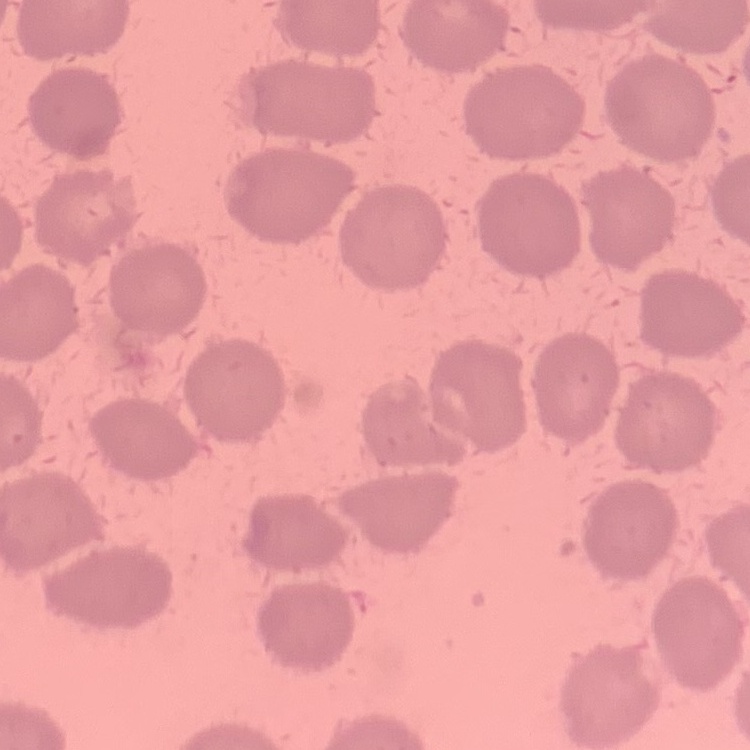 The red blood cells exhibit no rouleaux formation. Field's or Giemsa stain. One tile cut from a larger photomicrograph. Thin blood film.